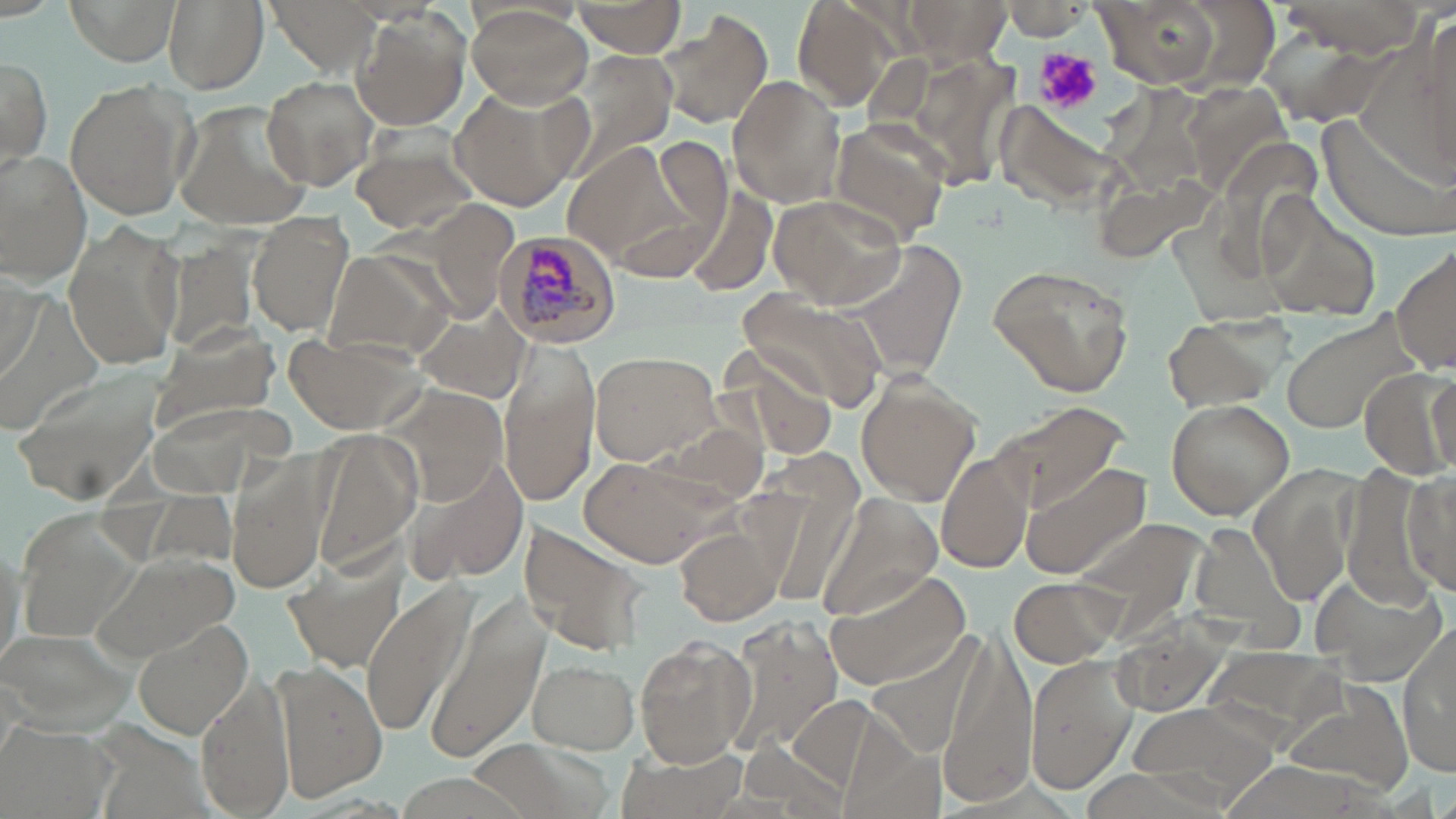
Approximate bounding boxes as named x1/y1/x2/y2 corners in pixels. Uninfected red blood cell locations: (x1=64, y1=0, x2=179, y2=66), (x1=163, y1=0, x2=268, y2=92), (x1=270, y1=0, x2=378, y2=70), (x1=792, y1=0, x2=899, y2=109), (x1=1093, y1=0, x2=1229, y2=90), (x1=1275, y1=0, x2=1432, y2=56), (x1=902, y1=1, x2=1011, y2=65), (x1=571, y1=2, x2=686, y2=58), (x1=1003, y1=3, x2=1088, y2=40), (x1=464, y1=5, x2=592, y2=107), (x1=351, y1=7, x2=472, y2=131), (x1=656, y1=11, x2=775, y2=132), (x1=0, y1=56, x2=50, y2=163), (x1=727, y1=74, x2=847, y2=209), (x1=261, y1=75, x2=377, y2=189), (x1=63, y1=79, x2=196, y2=222), (x1=447, y1=85, x2=589, y2=214), (x1=172, y1=102, x2=313, y2=231), (x1=998, y1=104, x2=1128, y2=212), (x1=1317, y1=114, x2=1455, y2=243), (x1=826, y1=118, x2=951, y2=244), (x1=349, y1=128, x2=484, y2=237), (x1=0, y1=151, x2=94, y2=283), (x1=682, y1=185, x2=780, y2=297), (x1=1255, y1=190, x2=1381, y2=320), (x1=770, y1=193, x2=908, y2=310), (x1=249, y1=212, x2=357, y2=336), (x1=61, y1=220, x2=187, y2=373), (x1=1390, y1=239, x2=1455, y2=379), (x1=839, y1=240, x2=970, y2=382), (x1=326, y1=251, x2=456, y2=360), (x1=987, y1=261, x2=1135, y2=397), (x1=736, y1=289, x2=887, y2=410), (x1=406, y1=304, x2=532, y2=402), (x1=1282, y1=309, x2=1421, y2=435), (x1=1161, y1=314, x2=1284, y2=417), (x1=145, y1=329, x2=279, y2=434), (x1=285, y1=335, x2=426, y2=436), (x1=501, y1=341, x2=599, y2=507), (x1=587, y1=350, x2=722, y2=466), (x1=10, y1=365, x2=169, y2=507), (x1=852, y1=371, x2=984, y2=506), (x1=1426, y1=374, x2=1454, y2=472), (x1=1164, y1=397, x2=1294, y2=519), (x1=989, y1=399, x2=1131, y2=515), (x1=308, y1=426, x2=422, y2=573), (x1=937, y1=448, x2=1034, y2=574), (x1=576, y1=456, x2=726, y2=567), (x1=408, y1=458, x2=530, y2=583), (x1=226, y1=461, x2=330, y2=594), (x1=1019, y1=462, x2=1152, y2=580), (x1=1403, y1=463, x2=1454, y2=599), (x1=812, y1=491, x2=943, y2=624), (x1=1077, y1=516, x2=1206, y2=635), (x1=1193, y1=521, x2=1298, y2=635), (x1=518, y1=523, x2=645, y2=654), (x1=675, y1=523, x2=787, y2=628), (x1=88, y1=549, x2=239, y2=661), (x1=281, y1=551, x2=404, y2=669), (x1=823, y1=565, x2=974, y2=691), (x1=1311, y1=572, x2=1446, y2=684), (x1=1007, y1=574, x2=1123, y2=667), (x1=361, y1=582, x2=473, y2=739), (x1=427, y1=600, x2=547, y2=765), (x1=131, y1=614, x2=253, y2=737), (x1=731, y1=618, x2=840, y2=754), (x1=0, y1=623, x2=141, y2=734), (x1=1397, y1=623, x2=1456, y2=775), (x1=938, y1=628, x2=1036, y2=805), (x1=635, y1=637, x2=756, y2=767), (x1=865, y1=638, x2=984, y2=758), (x1=1206, y1=646, x2=1348, y2=738), (x1=1024, y1=653, x2=1138, y2=795), (x1=526, y1=657, x2=641, y2=752), (x1=269, y1=659, x2=388, y2=800), (x1=194, y1=669, x2=295, y2=819), (x1=1278, y1=678, x2=1417, y2=797), (x1=789, y1=695, x2=888, y2=795), (x1=1127, y1=701, x2=1281, y2=807), (x1=1, y1=719, x2=121, y2=819), (x1=610, y1=738, x2=753, y2=819). Platelet locations: (x1=1037, y1=48, x2=1103, y2=114). Plasmodium malariae-infected red blood cell locations: (x1=488, y1=231, x2=624, y2=350). Slide-level diagnosis: Plasmodium malariae. Thin blood film. One field of a larger specimen. Image is 1456×819 pixels. Light microscopy. May-Grünwald-Giemsa stain. 1000x magnification.